Outline each blood parasite and name the species.
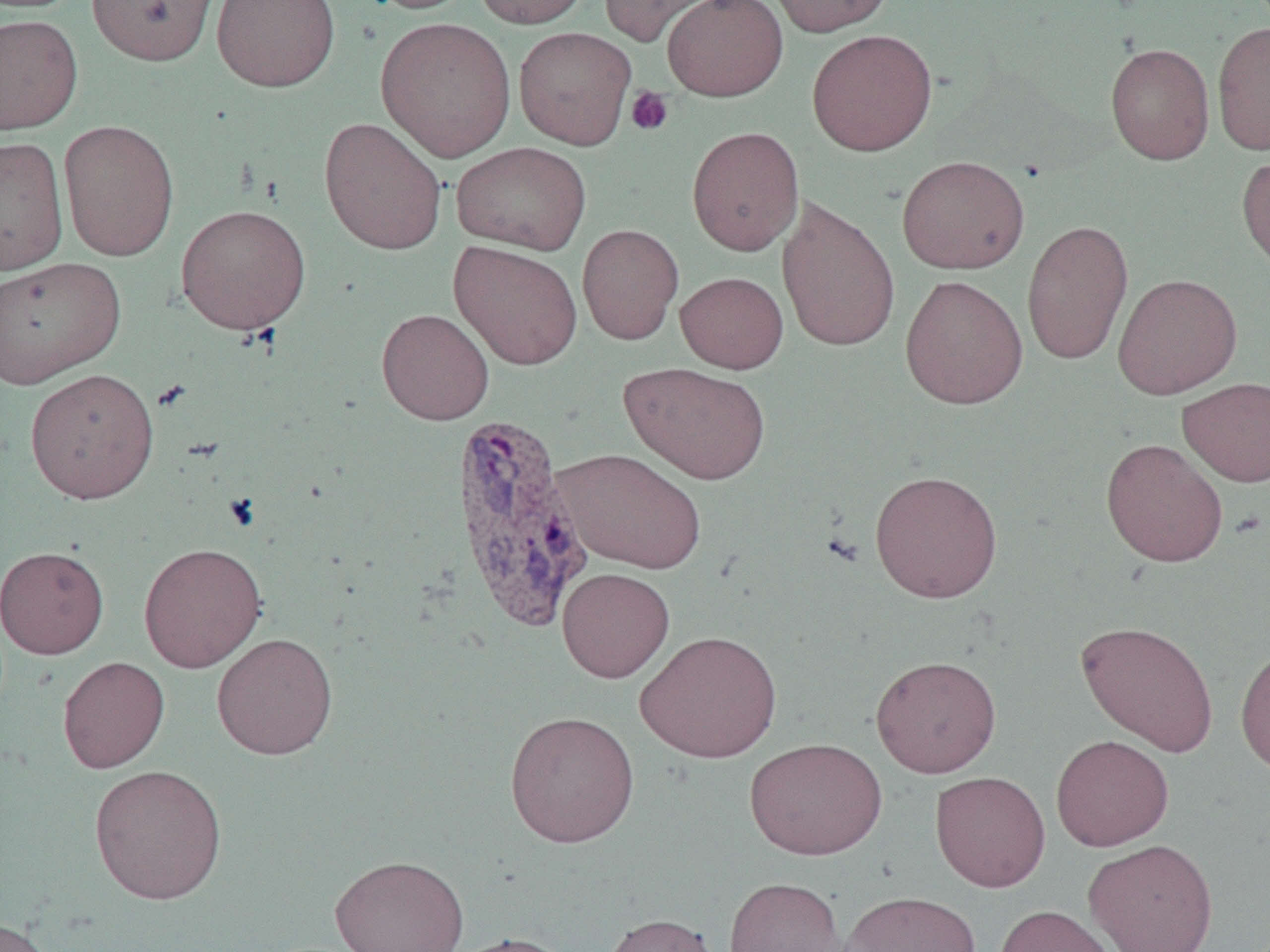
Approximate bounding boxes as (x1,y1)-(x2,y2) corner pairs in pixels.
Plasmodium vivax-infected red blood cells: (449,409)-(593,632).
No Plasmodium falciparum, Plasmodium ovale, Plasmodium malariae, Babesia divergens, or Trypanosoma brucei observed.

{
  "slide_level_diagnosis": "Plasmodium vivax",
  "preparation": "thin blood smear",
  "image_size": "1270×952 pixels",
  "platelet_locations": "approximate bounding boxes as (x1,y1)-(x2,y2) corner pairs in pixels: (625,86)-(674,136)",
  "magnification": "1000x",
  "field_of_view": "one of a larger specimen",
  "modality": "optical microscopy",
  "uninfected_red_blood_cell_locations": "approximate bounding boxes as (x1,y1)-(x2,y2) corner pairs in pixels: (87,0)-(217,65), (211,0)-(340,92), (357,0)-(482,14), (473,0)-(590,29), (599,0)-(724,47), (661,0)-(788,102), (765,0)-(895,36), (0,14)-(84,135), (375,16)-(517,163), (1211,21)-(1270,155), (513,26)-(636,150), (806,29)-(938,156), (1104,43)-(1215,165), (318,117)-(447,255), (58,119)-(179,262), (686,126)-(804,255), (0,136)-(69,276), (451,142)-(592,255), (1236,150)-(1270,274), (896,155)-(1029,274), (776,195)-(901,353), (175,203)-(311,335), (1022,218)-(1133,365), (577,223)-(684,345), (448,240)-(583,370), (0,256)-(126,389), (675,271)-(788,373), (1112,272)-(1243,399), (899,274)-(1028,410), (376,308)-(494,425), (619,362)-(771,485), (25,367)-(159,504), (1178,376)-(1270,487), (1100,438)-(1228,568), (553,448)-(707,574), (869,469)-(1003,603), (138,542)-(267,673), (0,545)-(109,659), (557,567)-(675,682), (1075,620)-(1219,756), (635,630)-(782,763), (211,632)-(338,760), (1235,643)-(1270,777), (870,655)-(1001,778), (57,656)-(170,773), (504,710)-(640,847), (1051,734)-(1174,851), (744,737)-(887,860), (89,763)-(228,905), (930,770)-(1051,891), (1084,838)-(1218,952), (329,853)-(469,952), (723,876)-(846,952), (839,890)-(981,952), (993,905)-(1119,952), (602,912)-(719,952), (0,918)-(56,952), (446,932)-(577,952)"
}